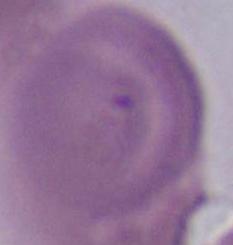
magnification = 1000x
identification = erythrocyte
modality = photomicrograph